Assess the morphology of the erythrocytes.
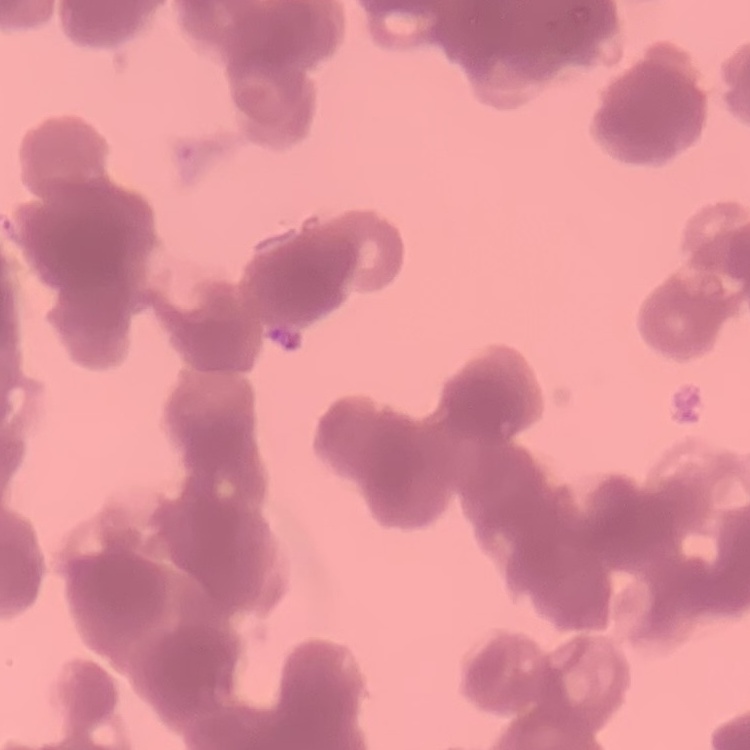
They show rouleaux formation.

preparation: thin peripheral smear
image_type: one tile cut from a larger photomicrograph
stain: Field's or Giemsa